Assess the morphology of the red blood cells.
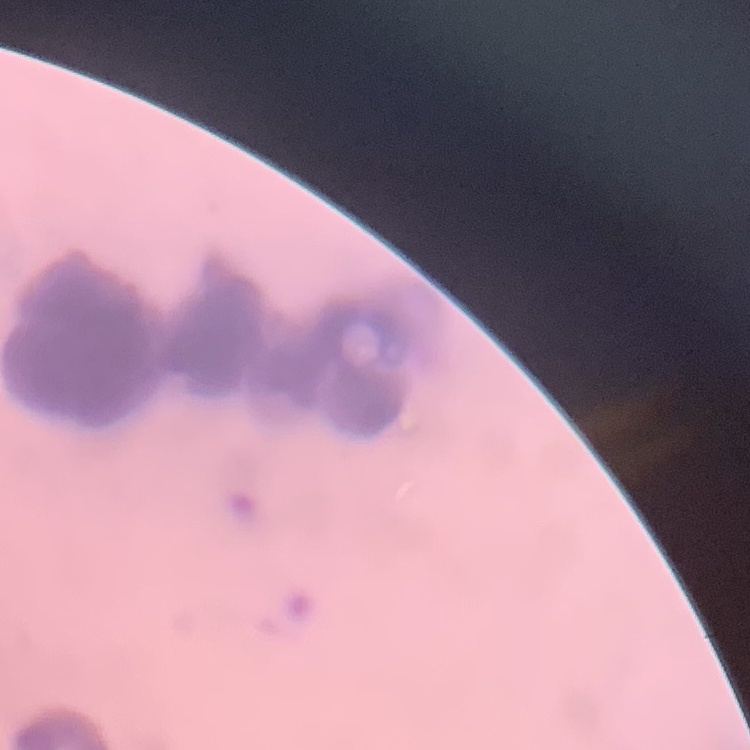
They show rouleaux formation.

Summary:
  - Image type: square crop of a larger photomicrograph
  - Preparation: thin blood smear
  - Stain: Field's or Giemsa